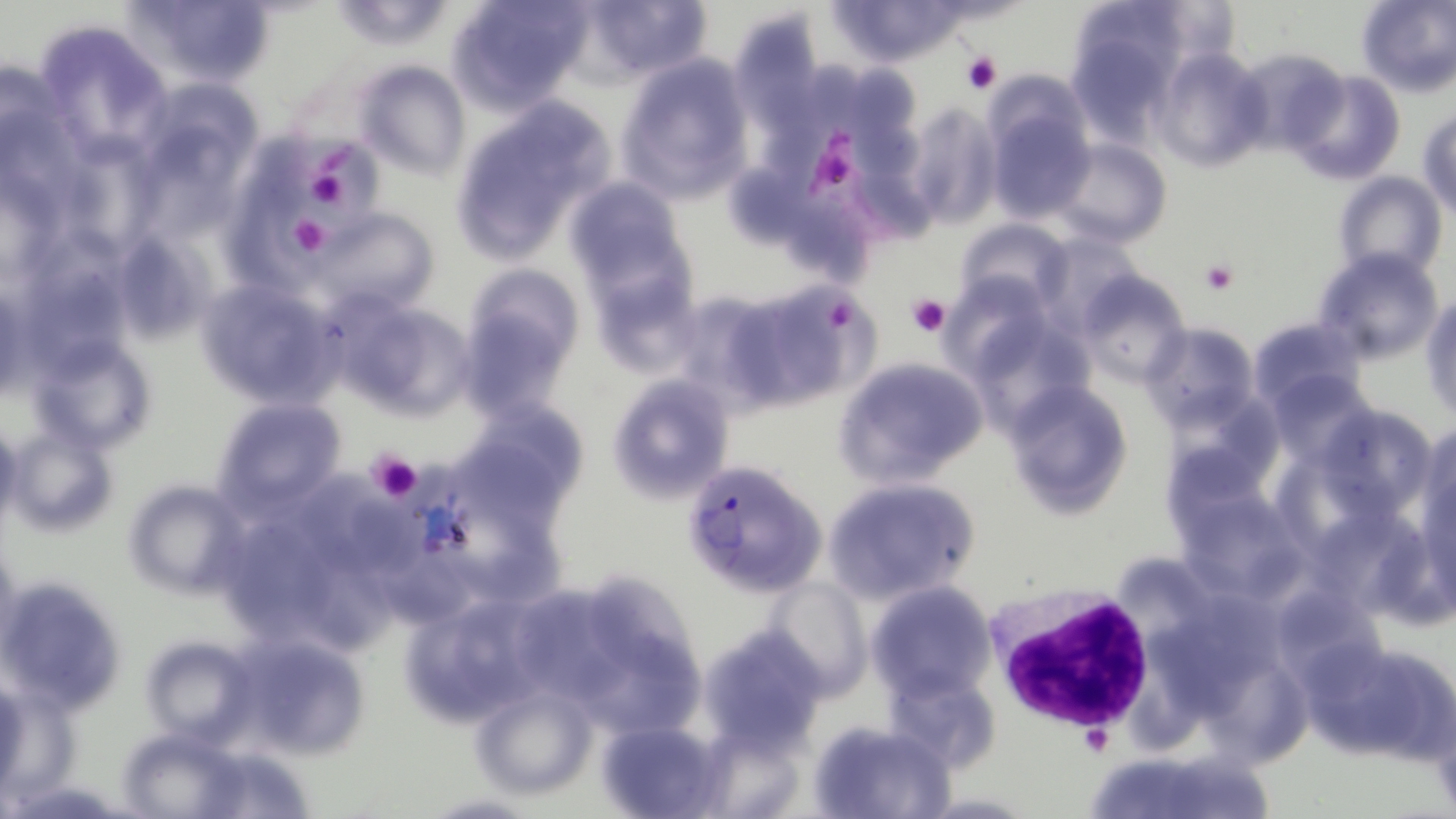
Approximate bounding boxes as (x1, y1, x2, y2) in pixels. Platelet locations: (960, 52, 1000, 93), (807, 145, 853, 201), (311, 173, 350, 209), (289, 215, 331, 258), (1199, 260, 1237, 295), (908, 293, 950, 338), (824, 303, 859, 338), (367, 447, 423, 501), (1079, 726, 1112, 757). Plasmodium falciparum-infected red blood cell locations: (678, 459, 825, 598). Uninfected red blood cell locations: (123, 0, 275, 91), (446, 0, 593, 114), (575, 0, 714, 83), (830, 0, 958, 68), (1356, 0, 1456, 97), (727, 10, 828, 146), (30, 22, 169, 158), (1070, 36, 1176, 146), (1150, 48, 1271, 172), (614, 53, 755, 201), (0, 58, 65, 172), (355, 61, 469, 178), (1288, 70, 1407, 185), (903, 102, 1001, 228), (454, 104, 608, 256), (986, 107, 1096, 222), (1419, 110, 1456, 216), (145, 131, 248, 251), (78, 134, 162, 256), (265, 135, 383, 245), (1053, 138, 1171, 249), (1335, 171, 1446, 282), (562, 177, 689, 292), (224, 197, 336, 306), (311, 208, 439, 315), (958, 219, 1071, 311), (137, 244, 212, 339), (1313, 248, 1442, 365), (39, 257, 133, 383), (461, 263, 587, 373), (586, 266, 700, 380), (1077, 272, 1191, 384), (727, 278, 875, 406), (196, 279, 343, 412), (671, 288, 796, 406), (1422, 294, 1455, 420), (348, 304, 481, 419), (1248, 315, 1366, 412), (1141, 323, 1258, 431), (39, 347, 151, 452), (833, 355, 991, 488), (606, 373, 734, 503), (1282, 378, 1377, 475), (1004, 381, 1130, 516), (214, 398, 345, 510), (459, 400, 589, 515), (0, 418, 21, 526), (1331, 418, 1420, 520), (1418, 423, 1456, 574), (8, 424, 116, 538), (1168, 449, 1272, 555), (311, 468, 425, 578), (1294, 469, 1402, 570), (822, 477, 979, 604), (121, 478, 251, 597), (1176, 482, 1303, 611), (444, 501, 562, 610), (232, 524, 323, 631), (1325, 524, 1413, 611), (311, 548, 406, 656), (547, 573, 708, 746), (0, 575, 125, 715), (762, 578, 870, 695), (867, 581, 995, 700), (396, 590, 545, 725), (1288, 602, 1381, 713), (697, 626, 829, 755), (139, 633, 257, 743), (233, 633, 371, 759), (1306, 635, 1454, 766), (1215, 667, 1321, 788), (880, 669, 1000, 774), (470, 679, 597, 799), (596, 719, 725, 819), (810, 719, 957, 819). White blood cell locations: (986, 587, 1159, 737). Slide-level diagnosis: Plasmodium falciparum. Single field of view. Light microscopy. Thin blood film. Image is 1456×819 pixels. Captured at 1000x magnification. May-Grünwald-Giemsa-stained preparation.